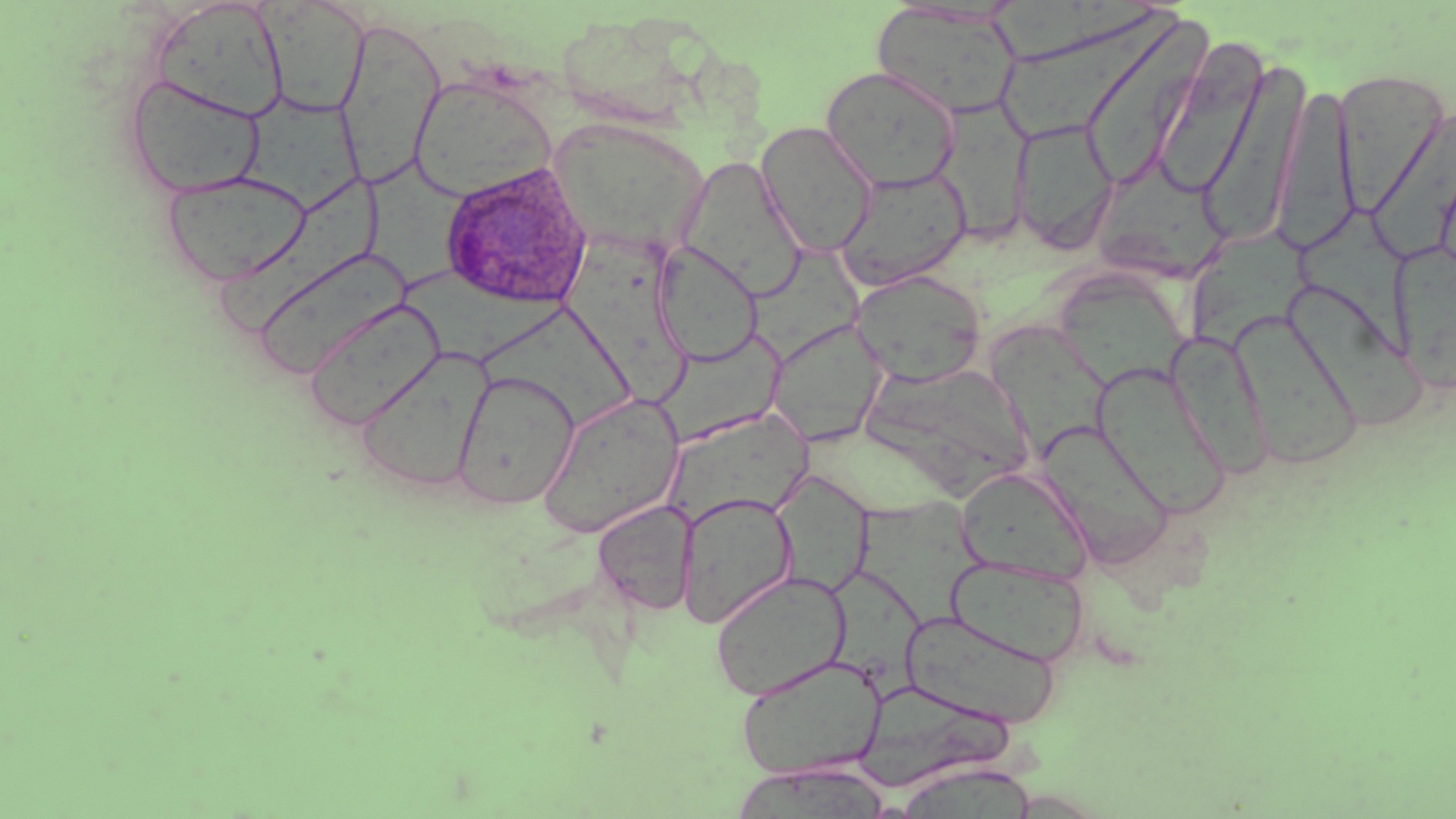
Summary:
  - Coordinate format: approximate bounding boxes as (x1, y1, x2, y2) in pixels
  - Uninfected red blood cell locations: (151, 1, 290, 123), (258, 1, 370, 118), (871, 4, 1024, 120), (997, 10, 1186, 137), (1077, 15, 1214, 192), (333, 17, 446, 189), (1151, 38, 1271, 200), (1197, 56, 1310, 244), (820, 66, 962, 192), (1333, 68, 1451, 219), (408, 74, 558, 200), (123, 75, 268, 199), (1274, 81, 1359, 254), (234, 93, 364, 214), (930, 100, 1033, 245), (1373, 103, 1456, 266), (548, 117, 710, 255), (1011, 117, 1118, 253), (755, 121, 878, 258), (367, 155, 479, 289), (679, 156, 808, 301), (1089, 165, 1223, 278), (835, 166, 973, 289), (161, 169, 312, 287), (210, 180, 394, 338), (1307, 212, 1414, 357), (1189, 226, 1323, 361), (567, 238, 693, 406), (1390, 239, 1456, 396), (652, 242, 763, 366), (265, 251, 420, 384), (1052, 268, 1194, 393), (851, 270, 987, 386), (399, 271, 575, 369), (1290, 287, 1424, 434), (298, 297, 444, 430), (481, 305, 629, 432), (1233, 316, 1364, 471), (769, 319, 888, 446), (991, 326, 1118, 456), (1163, 331, 1273, 479), (657, 332, 787, 447), (356, 349, 492, 492), (1092, 362, 1232, 521), (865, 367, 1035, 497), (452, 370, 580, 510), (538, 394, 684, 538), (672, 403, 828, 522), (1043, 425, 1173, 565), (956, 467, 1092, 584), (775, 471, 878, 603), (677, 491, 799, 628), (858, 494, 989, 628), (592, 500, 697, 616), (947, 557, 1090, 666), (823, 566, 929, 706), (709, 570, 852, 701), (903, 610, 1063, 728), (734, 654, 888, 779), (861, 683, 1024, 788), (740, 762, 886, 819), (905, 765, 1036, 819)
  - Plasmodium ovale-infected red blood cell locations: (440, 162, 593, 310)
  - Slide-level diagnosis: Plasmodium ovale
  - Stain: May-Grünwald-Giemsa
  - Preparation: thin blood film
  - Image size: 1456×819 pixels
  - Field of view: single
  - Modality: light microscopy
  - Magnification: 1000x